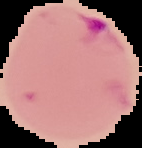 Result: Plasmodium parasites detected. From a thin blood smear. Image is 142×148 pixels. Segmented cell region on a black background.